Identify the cell.
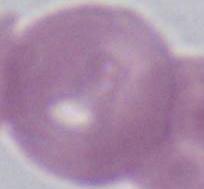
This is an erythrocyte.

Summary:
  - Magnification: 1000x
  - Modality: photomicrograph